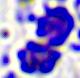

identification = leukocyte
modality = photomicrograph
magnification = 400x